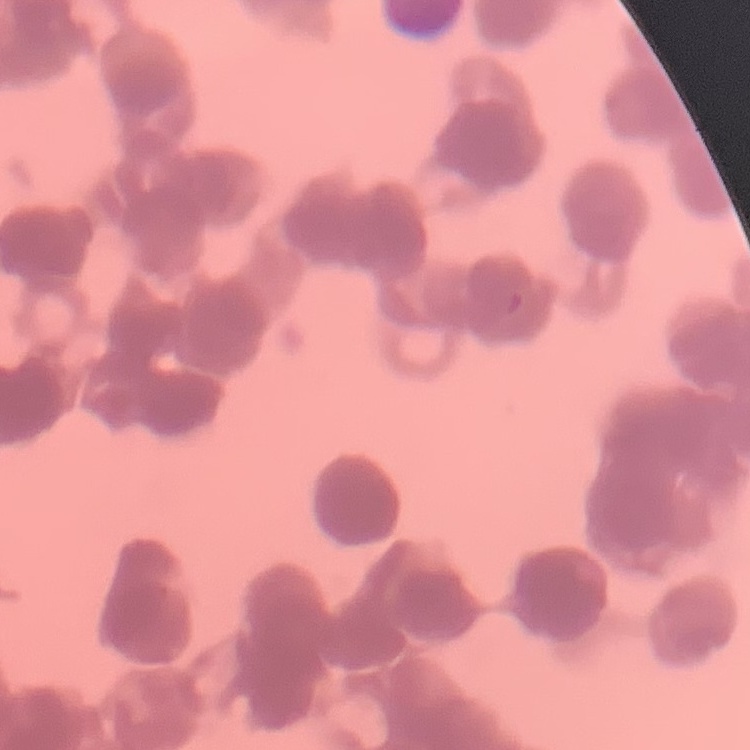

The erythrocytes show rouleaux formation. Field's or Giemsa stain. Square crop of a larger photomicrograph. Thin blood smear.